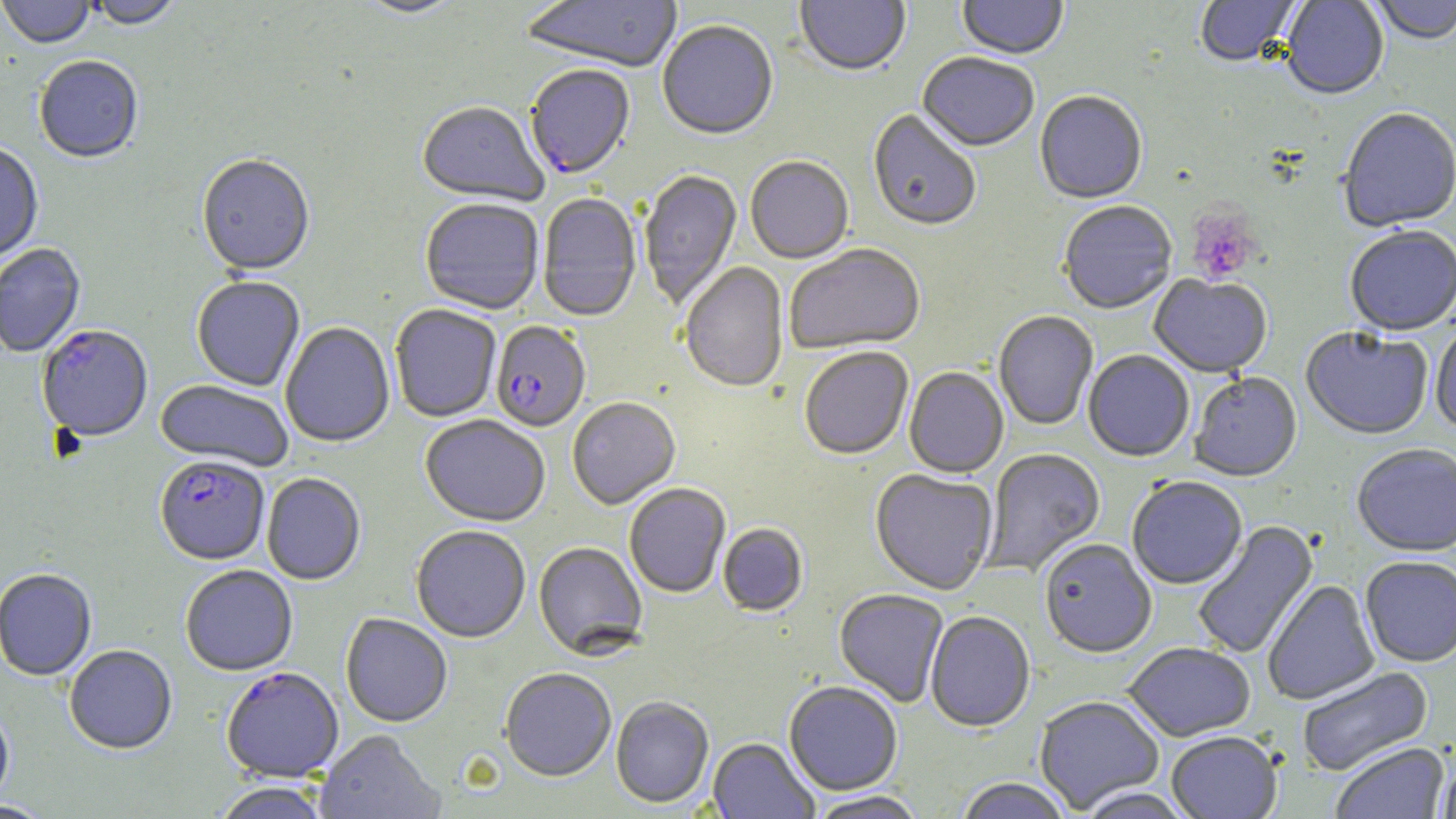
Summary:
  - Coordinate format: approximate bounding boxes as [x1, y1, x2, y2] in pixels
  - Platelet locations: [1186, 207, 1261, 284]
  - Uninfected red blood cell locations: [0, 0, 95, 51], [87, 0, 183, 31], [352, 0, 467, 20], [520, 0, 684, 75], [795, 0, 911, 79], [956, 0, 1068, 62], [1196, 0, 1300, 68], [1280, 0, 1389, 102], [1370, 0, 1456, 48], [657, 22, 778, 142], [917, 55, 1039, 154], [34, 58, 144, 165], [1034, 93, 1147, 206], [417, 103, 548, 208], [1337, 109, 1456, 234], [867, 111, 981, 234], [0, 143, 43, 263], [196, 156, 315, 278], [745, 158, 854, 265], [639, 170, 742, 311], [537, 194, 641, 323], [420, 200, 543, 316], [1059, 202, 1177, 316], [1345, 228, 1456, 338], [0, 243, 85, 359], [785, 245, 926, 356], [680, 263, 789, 395], [1149, 275, 1273, 380], [192, 277, 305, 392], [390, 306, 501, 423], [993, 312, 1099, 431], [1430, 321, 1456, 435], [280, 323, 395, 449], [1300, 328, 1432, 442], [799, 348, 913, 461], [1083, 351, 1194, 463], [904, 368, 1008, 479], [1189, 374, 1303, 484], [155, 381, 293, 472], [567, 398, 680, 510], [420, 416, 550, 528], [1351, 446, 1456, 558], [980, 449, 1107, 577], [870, 470, 998, 596], [262, 474, 366, 586], [1127, 478, 1247, 591], [624, 484, 731, 599], [1192, 521, 1319, 660], [718, 524, 808, 617], [411, 526, 530, 644], [1040, 541, 1157, 659], [533, 542, 648, 660], [1360, 558, 1456, 669], [180, 566, 298, 676], [0, 569, 97, 682], [1262, 581, 1380, 706], [834, 589, 949, 708], [925, 612, 1035, 733], [340, 613, 453, 728], [1124, 644, 1255, 742], [64, 645, 177, 756], [1296, 666, 1434, 778], [499, 669, 617, 782], [784, 681, 902, 796], [1034, 696, 1164, 814], [610, 697, 714, 809], [0, 703, 15, 812], [314, 731, 444, 819], [1167, 733, 1282, 819], [707, 739, 818, 819], [1331, 743, 1449, 819], [1436, 756, 1456, 819], [954, 779, 1073, 819], [211, 783, 332, 819], [1075, 786, 1196, 818], [805, 791, 930, 819], [1, 800, 56, 819]
  - Plasmodium falciparum-infected red blood cell locations: [523, 68, 635, 182], [491, 322, 590, 433], [37, 326, 154, 442], [155, 456, 270, 566], [221, 668, 344, 784]
  - Slide-level diagnosis: Plasmodium falciparum
  - Stain: May-Grünwald-Giemsa
  - Modality: light microscopy
  - Image size: 1456×819 pixels
  - Preparation: thin blood film
  - Magnification: 1000x
  - Field of view: single